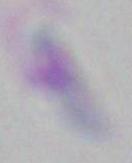
1000x magnification. Toxoplasma gondii is seen. Photomicrograph.